State the blood parasite species.
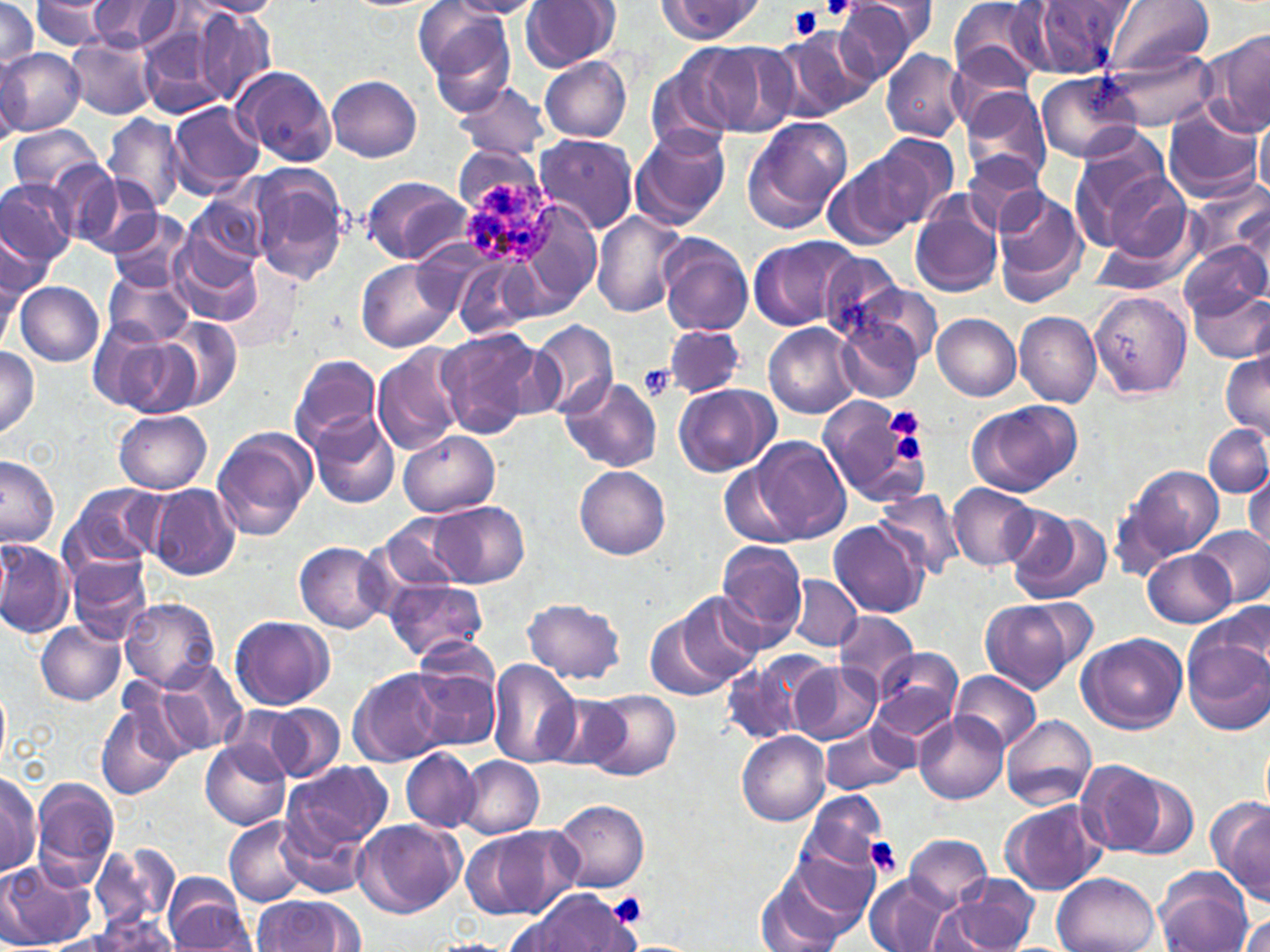
Plasmodium ovale.

{
  "modality": "optical microscopy",
  "plasmodium_ovale_infected_red_blood_cell_locations": "approximate bounding boxes as [x1, y1, x2, y2] in pixels: [465, 177, 557, 266]",
  "field_of_view": "single",
  "image_size": "1270×952 pixels",
  "uninfected_red_blood_cell_locations": "approximate bounding boxes as [x1, y1, x2, y2] in pixels: [0, 0, 43, 75], [85, 0, 185, 54], [185, 0, 283, 18], [448, 0, 545, 18], [520, 0, 619, 72], [836, 0, 922, 81], [860, 0, 938, 49], [947, 0, 1047, 86], [1025, 0, 1135, 80], [1108, 0, 1212, 76], [659, 1, 760, 42], [28, 2, 127, 51], [193, 5, 276, 104], [417, 6, 517, 106], [140, 26, 230, 118], [772, 27, 877, 122], [1204, 30, 1270, 138], [65, 36, 158, 120], [704, 41, 796, 135], [950, 46, 1035, 123], [1106, 46, 1217, 129], [0, 48, 83, 135], [882, 48, 968, 141], [0, 51, 29, 147], [540, 56, 632, 142], [646, 60, 738, 155], [232, 65, 339, 167], [1035, 73, 1144, 160], [327, 75, 422, 162], [452, 82, 550, 161], [963, 89, 1053, 186], [168, 101, 262, 196], [1161, 102, 1262, 201], [1256, 112, 1270, 198], [104, 113, 186, 215], [741, 116, 852, 233], [6, 125, 105, 196], [630, 127, 731, 230], [531, 133, 636, 235], [863, 133, 959, 227], [1068, 147, 1172, 254], [962, 153, 1048, 236], [823, 159, 919, 251], [245, 165, 349, 284], [53, 166, 155, 254], [1104, 171, 1192, 258], [360, 175, 471, 264], [0, 177, 77, 272], [6, 179, 85, 362], [1189, 182, 1269, 269], [990, 188, 1085, 303], [186, 195, 271, 273], [508, 201, 602, 319], [910, 201, 1004, 297], [590, 209, 687, 318], [109, 211, 194, 292], [1, 229, 46, 328], [170, 232, 261, 327], [657, 234, 754, 336], [748, 235, 860, 332], [1177, 240, 1269, 319], [812, 247, 907, 342], [453, 255, 547, 338], [357, 260, 457, 353], [102, 269, 192, 346], [847, 280, 943, 371], [16, 281, 104, 366], [1190, 285, 1270, 363], [1088, 290, 1191, 397], [1016, 312, 1101, 406], [933, 314, 1022, 400], [835, 315, 925, 403], [159, 316, 244, 411], [529, 319, 618, 418], [90, 321, 198, 418], [763, 323, 859, 418], [664, 325, 745, 399], [436, 327, 548, 438], [373, 345, 467, 456], [0, 346, 40, 435], [1221, 352, 1270, 440], [289, 354, 382, 451], [558, 376, 662, 472], [674, 384, 775, 479], [818, 395, 932, 510], [966, 398, 1082, 497], [113, 409, 212, 494], [307, 412, 401, 509], [1204, 425, 1270, 499], [212, 428, 316, 541], [399, 432, 499, 517], [754, 438, 850, 546], [0, 456, 59, 546], [719, 461, 798, 547], [1117, 464, 1225, 568], [576, 466, 671, 559], [1246, 472, 1270, 554], [63, 481, 165, 573], [147, 483, 242, 580], [949, 484, 1039, 572], [873, 488, 966, 580], [426, 501, 529, 588], [1004, 506, 1111, 606], [373, 513, 471, 596], [829, 521, 928, 618], [1193, 526, 1270, 607], [0, 537, 72, 641], [716, 539, 809, 647], [294, 541, 390, 633], [1143, 549, 1236, 628], [66, 553, 154, 645], [788, 574, 862, 651], [385, 577, 488, 663], [673, 591, 761, 688], [120, 598, 221, 691], [521, 598, 627, 686], [979, 598, 1086, 692], [1197, 600, 1266, 689], [647, 611, 734, 701], [834, 611, 918, 692], [229, 615, 335, 711], [841, 620, 943, 730], [36, 622, 126, 706], [1078, 632, 1189, 735], [1184, 635, 1269, 734], [870, 646, 963, 741], [404, 649, 503, 754], [156, 660, 250, 756], [487, 660, 579, 768], [720, 661, 803, 744], [788, 661, 882, 745], [349, 668, 450, 766], [951, 671, 1040, 751], [0, 686, 10, 767], [95, 689, 191, 800], [583, 690, 681, 782], [541, 692, 636, 773], [254, 702, 346, 783], [913, 710, 1007, 804], [1000, 714, 1097, 810], [819, 721, 917, 797], [738, 731, 829, 827], [200, 740, 291, 830], [401, 748, 479, 833], [457, 756, 544, 839], [1075, 759, 1166, 857], [1050, 761, 1172, 920], [284, 762, 392, 852], [0, 769, 42, 877], [1121, 773, 1199, 859], [30, 778, 119, 885], [798, 790, 889, 878], [1208, 796, 1270, 904], [551, 799, 649, 893], [1001, 800, 1107, 895], [278, 805, 377, 895], [225, 815, 312, 907], [352, 818, 466, 918], [461, 826, 580, 920], [785, 831, 886, 928], [906, 834, 992, 909], [91, 844, 179, 931], [0, 861, 92, 949], [1156, 867, 1254, 952], [759, 873, 850, 952], [863, 873, 954, 952], [1053, 873, 1160, 952], [939, 874, 1041, 951], [167, 880, 257, 950], [511, 886, 643, 952], [252, 895, 361, 951], [1236, 912, 1270, 952], [86, 913, 182, 951], [421, 938, 519, 952]",
  "magnification": "1000x",
  "stain": "May-Grünwald-Giemsa",
  "platelet_locations": "approximate bounding boxes as [x1, y1, x2, y2] in pixels: [821, 0, 856, 22], [788, 6, 824, 38], [639, 364, 673, 400], [889, 409, 923, 437], [894, 436, 925, 462], [866, 837, 903, 877], [609, 892, 649, 926]",
  "preparation": "thin blood film"
}